Identify the blood parasite species.
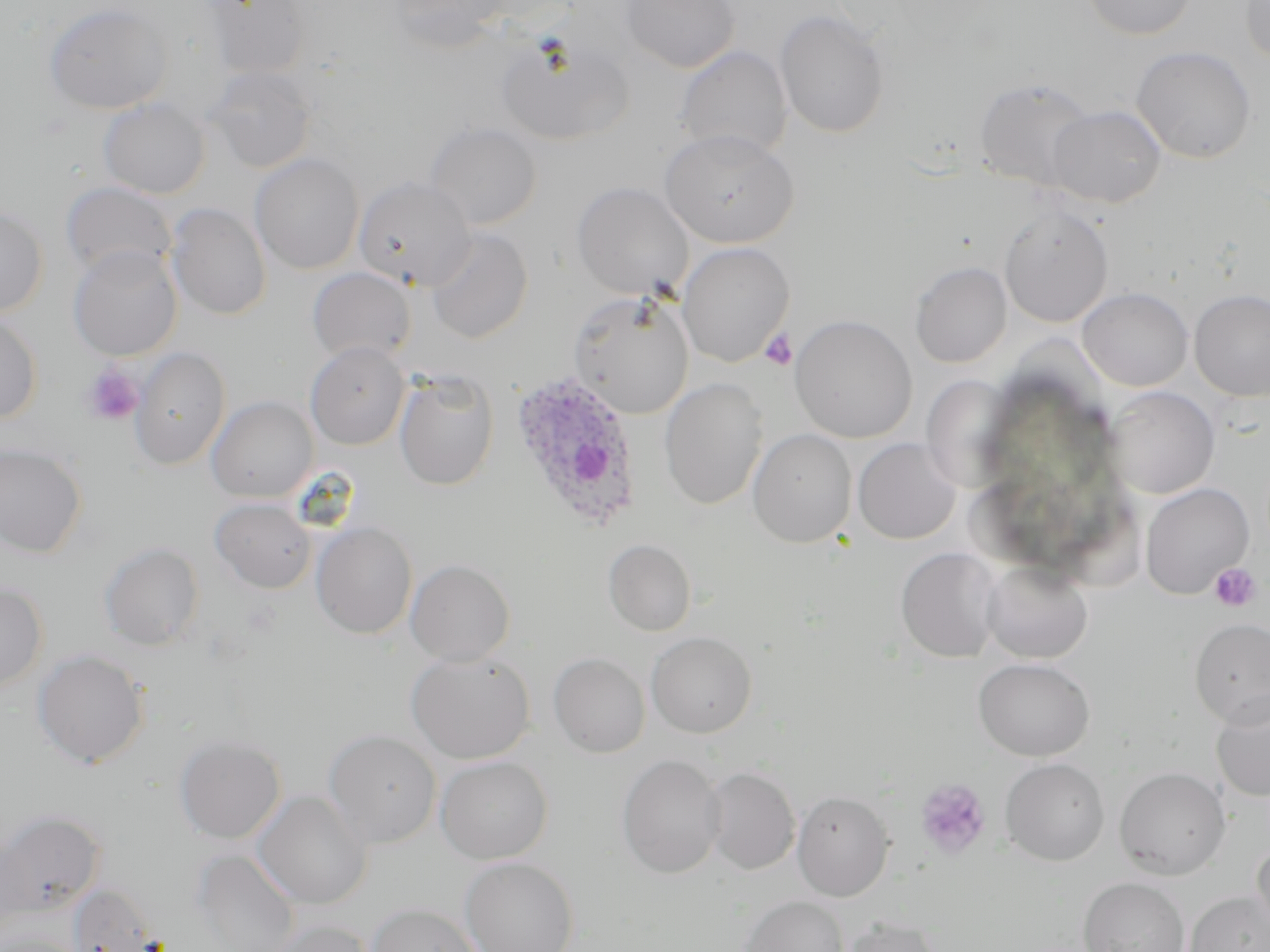
Plasmodium ovale.

uninfected red blood cell locations = approximate bounding boxes as (x1,y1)-(x2,y2) corner pairs in pixels: (203,0)-(312,78), (387,0)-(510,50), (621,0)-(739,72), (1083,0)-(1195,38), (1240,1)-(1270,66), (44,2)-(171,114), (774,9)-(890,138), (496,35)-(634,146), (675,46)-(792,159), (1132,46)-(1257,163), (205,66)-(316,172), (974,77)-(1096,191), (98,98)-(211,199), (1047,105)-(1166,208), (425,122)-(542,230), (660,128)-(799,248), (250,153)-(364,274), (353,176)-(475,290), (572,181)-(692,298), (60,182)-(176,281), (166,202)-(271,320), (999,203)-(1113,327), (0,205)-(49,317), (426,227)-(533,344), (676,241)-(795,367), (68,245)-(182,361), (910,261)-(1012,368), (307,267)-(416,363), (1078,287)-(1193,391), (1189,289)-(1270,401), (568,291)-(694,419), (0,313)-(42,423), (789,314)-(916,443), (306,341)-(410,449), (131,347)-(231,470), (395,371)-(500,490), (921,375)-(1019,491), (659,378)-(768,510), (1104,386)-(1219,498), (206,396)-(319,502), (748,428)-(857,548), (853,438)-(961,544), (0,442)-(88,558), (1140,483)-(1254,598), (210,498)-(316,593), (311,521)-(418,638), (603,538)-(696,636), (99,541)-(205,651), (896,547)-(1003,663), (405,559)-(515,666), (981,561)-(1093,663), (0,581)-(48,690), (1189,617)-(1270,727), (645,631)-(757,737), (32,649)-(149,768), (406,650)-(535,764), (548,652)-(650,757), (973,658)-(1094,761), (1211,691)-(1270,803), (323,729)-(442,848), (174,734)-(286,843), (617,753)-(726,878), (435,756)-(553,864), (1000,758)-(1109,865), (702,766)-(801,874), (1114,767)-(1231,879), (253,790)-(372,909), (792,790)-(894,901), (0,810)-(106,915), (0,837)-(34,934), (1251,839)-(1270,941), (192,849)-(299,952), (460,857)-(579,952), (1078,877)-(1190,952), (69,882)-(165,952), (1184,890)-(1269,952), (738,896)-(849,952), (367,902)-(481,952), (838,916)-(942,952), (266,918)-(375,952), (0,931)-(82,952)
Plasmodium ovale-infected red blood cell locations = approximate bounding boxes as (x1,y1)-(x2,y2) corner pairs in pixels: (509,370)-(642,532)
modality = optical microscopy
platelet locations = approximate bounding boxes as (x1,y1)-(x2,y2) corner pairs in pixels: (760,328)-(797,370), (81,364)-(144,427), (1209,563)-(1260,611), (915,778)-(990,857)
preparation = thin blood smear
magnification = 1000x
image size = 1270×952 pixels
field of view = one of a larger specimen
stain = May-Grünwald-Giemsa